Identify the parasite.
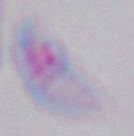
This is Toxoplasma gondii.

Summary:
  - Magnification: 1000x
  - Modality: photomicrograph